Assess this cell for malaria.
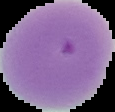

Parasitized.

preparation: thin blood film
image_size: 115×112 pixels
image_type: segmented cell region on a black background